Evaluate for Plasmodium parasites.
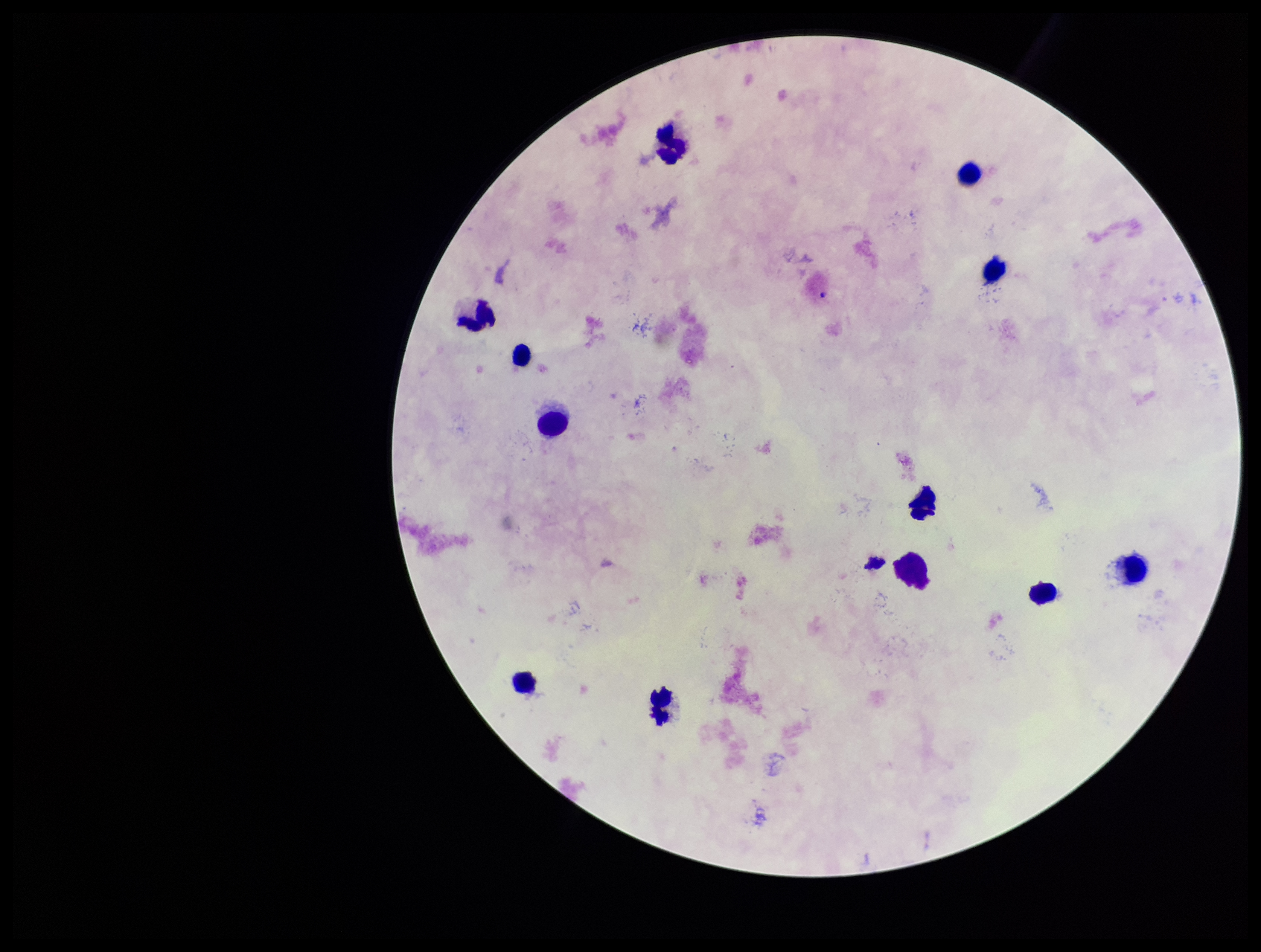
None detected.

Parasite count: 0. Preparation: thick blood smear. Leukocyte count: 12. Giemsa stain. Photographed through the microscope eyepiece with a smartphone camera. One field from this slide. Image is 1261×952 pixels. Patient malaria status: negative.